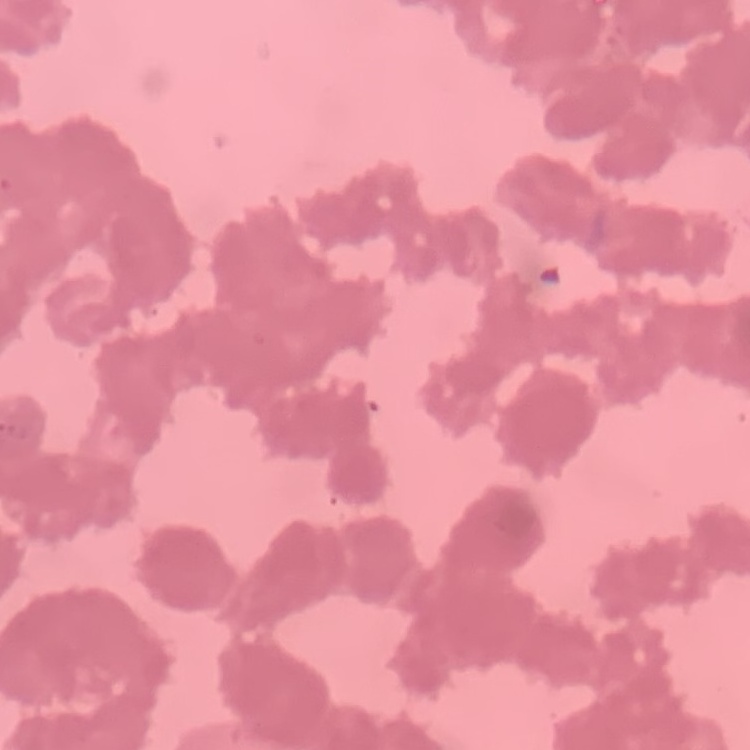

red_blood_cell_morphology: rouleaux formation
image_type: one tile cut from a larger photomicrograph
preparation: thin blood film
stain: Field's or Giemsa